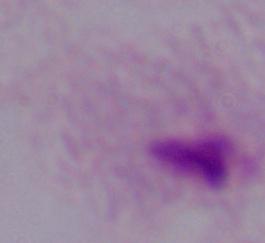

magnification = 1000x
identification = trichomonad
modality = micrograph